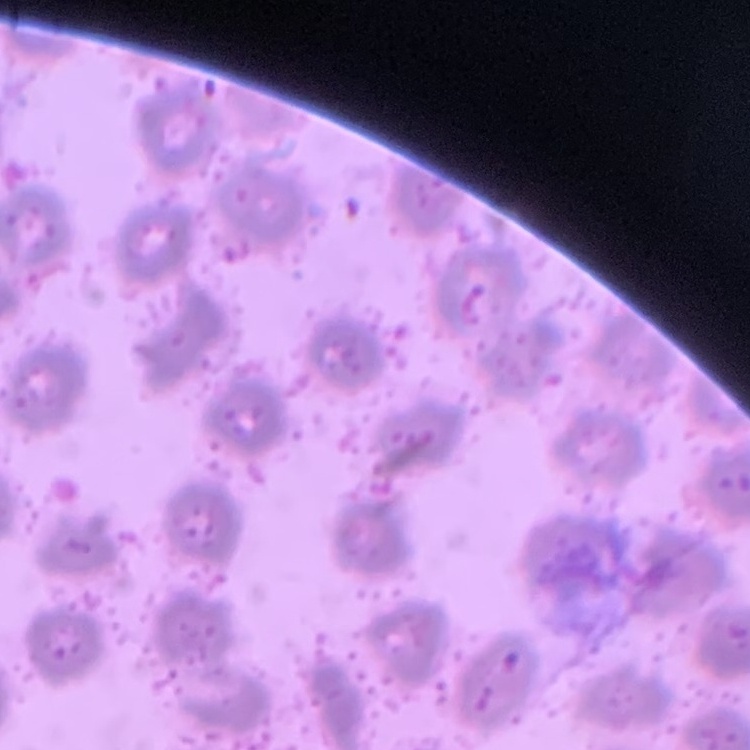
Summary:
  - Erythrocyte morphology: no rouleaux formation
  - Preparation: thin peripheral smear
  - Image type: one tile cut from a larger photomicrograph
  - Stain: Field's or Giemsa